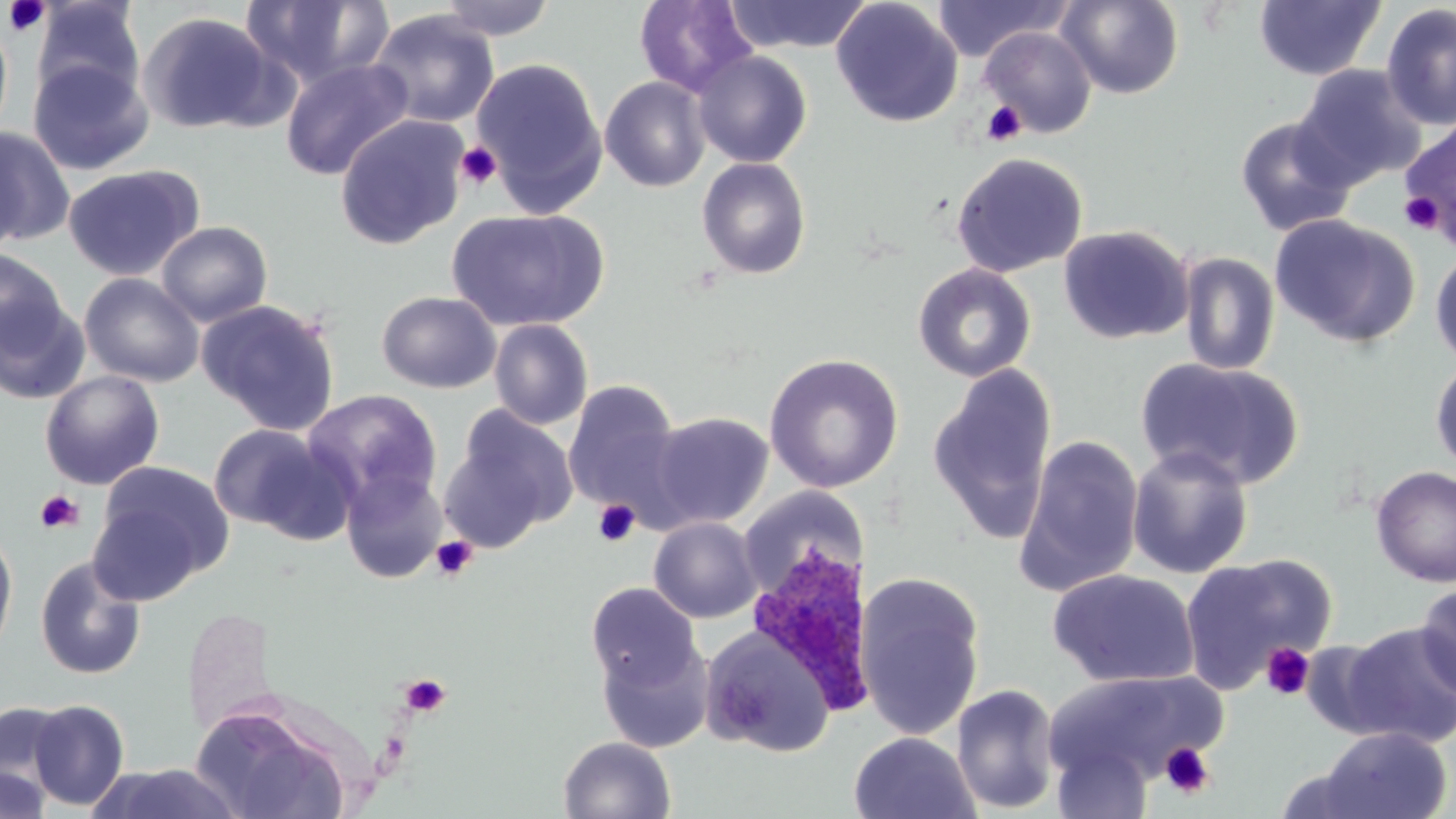

Approximate bounding boxes as (x1, y1, x2, y2) in pixels. Uninfected red blood cell locations: (238, 0, 395, 90), (436, 0, 556, 40), (723, 0, 873, 54), (831, 0, 963, 128), (931, 0, 1069, 62), (1057, 0, 1184, 99), (31, 1, 145, 106), (634, 1, 756, 96), (1253, 1, 1386, 80), (1380, 3, 1455, 131), (368, 10, 500, 128), (138, 11, 280, 134), (0, 18, 14, 142), (979, 27, 1097, 138), (691, 49, 812, 168), (27, 57, 153, 176), (281, 58, 414, 181), (471, 58, 608, 213), (1293, 64, 1426, 189), (600, 76, 711, 192), (334, 114, 468, 250), (1234, 116, 1356, 237), (1398, 119, 1456, 243), (0, 127, 75, 247), (0, 136, 27, 259), (950, 152, 1088, 277), (696, 156, 812, 280), (63, 165, 202, 281), (447, 207, 609, 332), (1269, 215, 1420, 348), (156, 221, 273, 327), (1058, 224, 1194, 344), (1430, 246, 1456, 370), (0, 249, 68, 355), (1178, 252, 1280, 376), (913, 263, 1036, 382), (79, 273, 205, 387), (376, 290, 501, 393), (0, 298, 91, 405), (196, 299, 341, 436), (489, 319, 593, 430), (764, 353, 904, 493), (1430, 355, 1456, 476), (1136, 357, 1303, 490), (927, 365, 1059, 546), (40, 371, 165, 490), (562, 380, 685, 515), (302, 389, 443, 511), (438, 407, 576, 553), (649, 412, 773, 529), (208, 424, 341, 537), (1015, 435, 1145, 596), (1127, 446, 1254, 580), (88, 461, 233, 599), (1370, 465, 1456, 587), (341, 469, 446, 584), (738, 486, 869, 597), (648, 517, 762, 623), (0, 526, 18, 664), (1180, 554, 1337, 694), (35, 556, 146, 681), (1047, 570, 1200, 689), (855, 573, 985, 740), (1415, 581, 1456, 700), (586, 582, 701, 692), (1335, 622, 1456, 747), (701, 626, 837, 757), (597, 639, 714, 753), (1048, 670, 1225, 786), (951, 683, 1061, 814), (190, 698, 352, 819), (27, 699, 130, 810), (0, 702, 71, 800), (1317, 726, 1452, 819), (848, 731, 980, 819), (558, 736, 676, 818), (1051, 742, 1153, 819), (90, 763, 246, 819), (0, 766, 51, 819), (1271, 766, 1384, 818). Plasmodium ovale-infected red blood cell locations: (747, 542, 880, 717). Platelet locations: (3, 0, 50, 37), (982, 101, 1026, 146), (456, 141, 503, 189), (1399, 191, 1446, 235), (35, 490, 83, 534), (593, 500, 640, 547), (431, 536, 478, 581), (1260, 642, 1315, 701), (399, 674, 451, 718), (1159, 742, 1217, 800). Slide-level diagnosis: Plasmodium ovale. Thin blood film. Optical microscopy. 1000x magnification. Single field of view. Image is 1456×819 pixels. May-Grünwald-Giemsa-stained preparation.